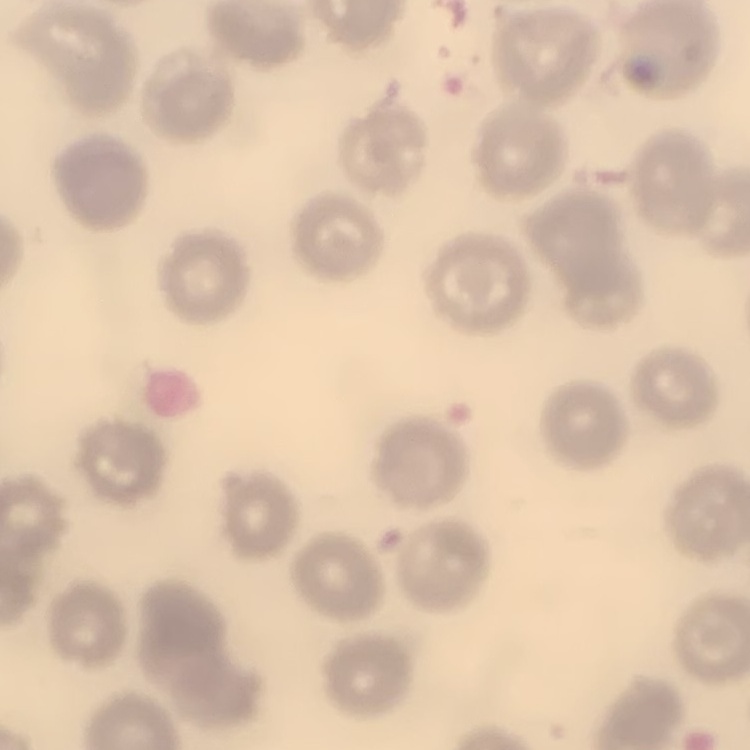

The red blood cells exhibit no rouleaux formation. Square crop of a larger photomicrograph. Stained with either Field's or Giemsa. Thin peripheral smear.